Locate and identify every blood parasite.
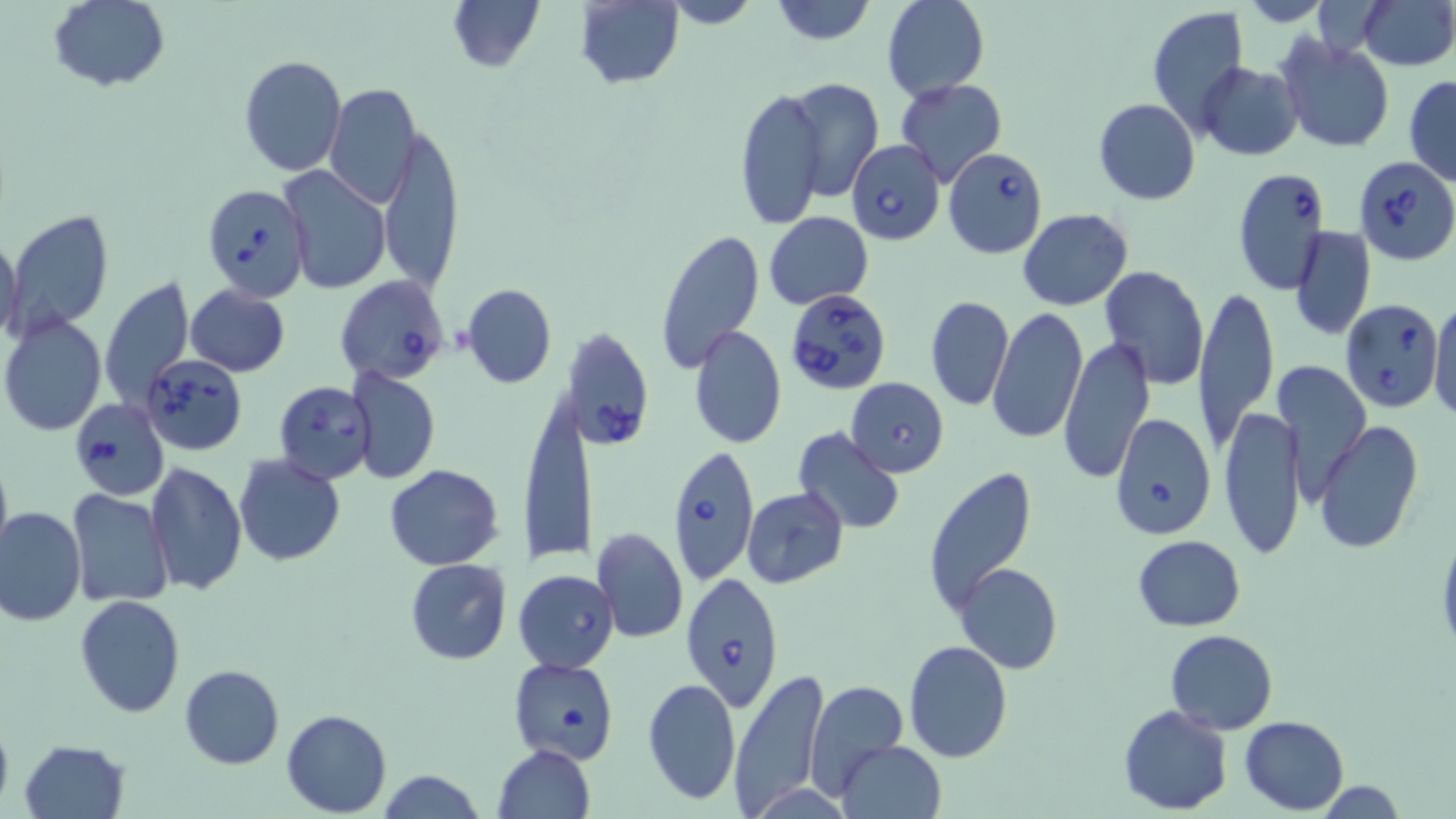
Approximate bounding boxes as named x1/y1/x2/y2 corners in pixels.
Babesia divergens-infected red blood cells: (x1=846, y1=140, x2=945, y2=244), (x1=942, y1=147, x2=1048, y2=258), (x1=1355, y1=156, x2=1455, y2=265), (x1=1232, y1=167, x2=1330, y2=293), (x1=202, y1=182, x2=312, y2=301), (x1=335, y1=276, x2=448, y2=385), (x1=785, y1=288, x2=894, y2=398), (x1=1340, y1=298, x2=1443, y2=412), (x1=564, y1=325, x2=657, y2=451), (x1=142, y1=355, x2=246, y2=456), (x1=272, y1=380, x2=375, y2=486), (x1=69, y1=398, x2=169, y2=500), (x1=1110, y1=412, x2=1216, y2=539), (x1=668, y1=442, x2=760, y2=584), (x1=680, y1=572, x2=786, y2=711).
No Plasmodium falciparum, Plasmodium ovale, Plasmodium malariae, Plasmodium vivax, or Trypanosoma brucei observed.

Summary:
  - Uninfected red blood cell locations: (x1=47, y1=0, x2=170, y2=93), (x1=448, y1=0, x2=545, y2=72), (x1=660, y1=0, x2=763, y2=29), (x1=767, y1=0, x2=877, y2=47), (x1=881, y1=0, x2=989, y2=101), (x1=1237, y1=0, x2=1335, y2=25), (x1=1356, y1=0, x2=1455, y2=70), (x1=576, y1=1, x2=684, y2=89), (x1=1146, y1=5, x2=1249, y2=131), (x1=1276, y1=35, x2=1394, y2=154), (x1=239, y1=54, x2=348, y2=176), (x1=1196, y1=63, x2=1302, y2=160), (x1=1404, y1=74, x2=1456, y2=186), (x1=783, y1=77, x2=885, y2=202), (x1=896, y1=78, x2=1007, y2=188), (x1=324, y1=83, x2=421, y2=206), (x1=736, y1=86, x2=828, y2=230), (x1=1093, y1=98, x2=1201, y2=205), (x1=376, y1=122, x2=463, y2=295), (x1=278, y1=165, x2=390, y2=296), (x1=1017, y1=208, x2=1134, y2=311), (x1=6, y1=209, x2=114, y2=336), (x1=764, y1=211, x2=873, y2=308), (x1=1288, y1=226, x2=1375, y2=343), (x1=1, y1=227, x2=23, y2=350), (x1=656, y1=229, x2=765, y2=373), (x1=1099, y1=264, x2=1209, y2=390), (x1=100, y1=275, x2=196, y2=412), (x1=462, y1=283, x2=558, y2=388), (x1=185, y1=285, x2=291, y2=376), (x1=1194, y1=287, x2=1279, y2=453), (x1=925, y1=295, x2=1014, y2=411), (x1=1430, y1=297, x2=1456, y2=420), (x1=989, y1=306, x2=1088, y2=443), (x1=2, y1=315, x2=106, y2=437), (x1=688, y1=324, x2=787, y2=450), (x1=1060, y1=336, x2=1156, y2=483), (x1=1273, y1=360, x2=1372, y2=507), (x1=348, y1=369, x2=440, y2=484), (x1=845, y1=377, x2=949, y2=477), (x1=519, y1=392, x2=594, y2=568), (x1=1220, y1=405, x2=1304, y2=560), (x1=1315, y1=422, x2=1424, y2=553), (x1=790, y1=427, x2=906, y2=534), (x1=0, y1=446, x2=13, y2=564), (x1=234, y1=455, x2=345, y2=566), (x1=144, y1=461, x2=247, y2=597), (x1=385, y1=464, x2=504, y2=569), (x1=922, y1=467, x2=1037, y2=618), (x1=741, y1=488, x2=848, y2=589), (x1=67, y1=491, x2=173, y2=607), (x1=1, y1=506, x2=86, y2=626), (x1=590, y1=526, x2=689, y2=644), (x1=1133, y1=534, x2=1245, y2=632), (x1=405, y1=558, x2=512, y2=666), (x1=955, y1=563, x2=1063, y2=675), (x1=513, y1=569, x2=620, y2=673), (x1=75, y1=594, x2=187, y2=717), (x1=1166, y1=629, x2=1278, y2=735), (x1=902, y1=641, x2=1013, y2=763), (x1=508, y1=656, x2=620, y2=765), (x1=180, y1=665, x2=284, y2=769), (x1=729, y1=668, x2=829, y2=814), (x1=641, y1=676, x2=741, y2=807), (x1=804, y1=678, x2=910, y2=795), (x1=1118, y1=704, x2=1233, y2=814), (x1=0, y1=707, x2=14, y2=816), (x1=281, y1=708, x2=392, y2=816), (x1=1240, y1=716, x2=1349, y2=814), (x1=17, y1=738, x2=131, y2=819), (x1=836, y1=740, x2=947, y2=819), (x1=493, y1=744, x2=595, y2=818), (x1=377, y1=768, x2=485, y2=819), (x1=1313, y1=780, x2=1408, y2=817)
  - Slide-level diagnosis: Babesia divergens
  - Magnification: 1000x
  - Image size: 1456×819 pixels
  - Modality: light microscopy
  - Stain: May-Grünwald-Giemsa
  - Field of view: one of a larger specimen
  - Preparation: thin blood smear